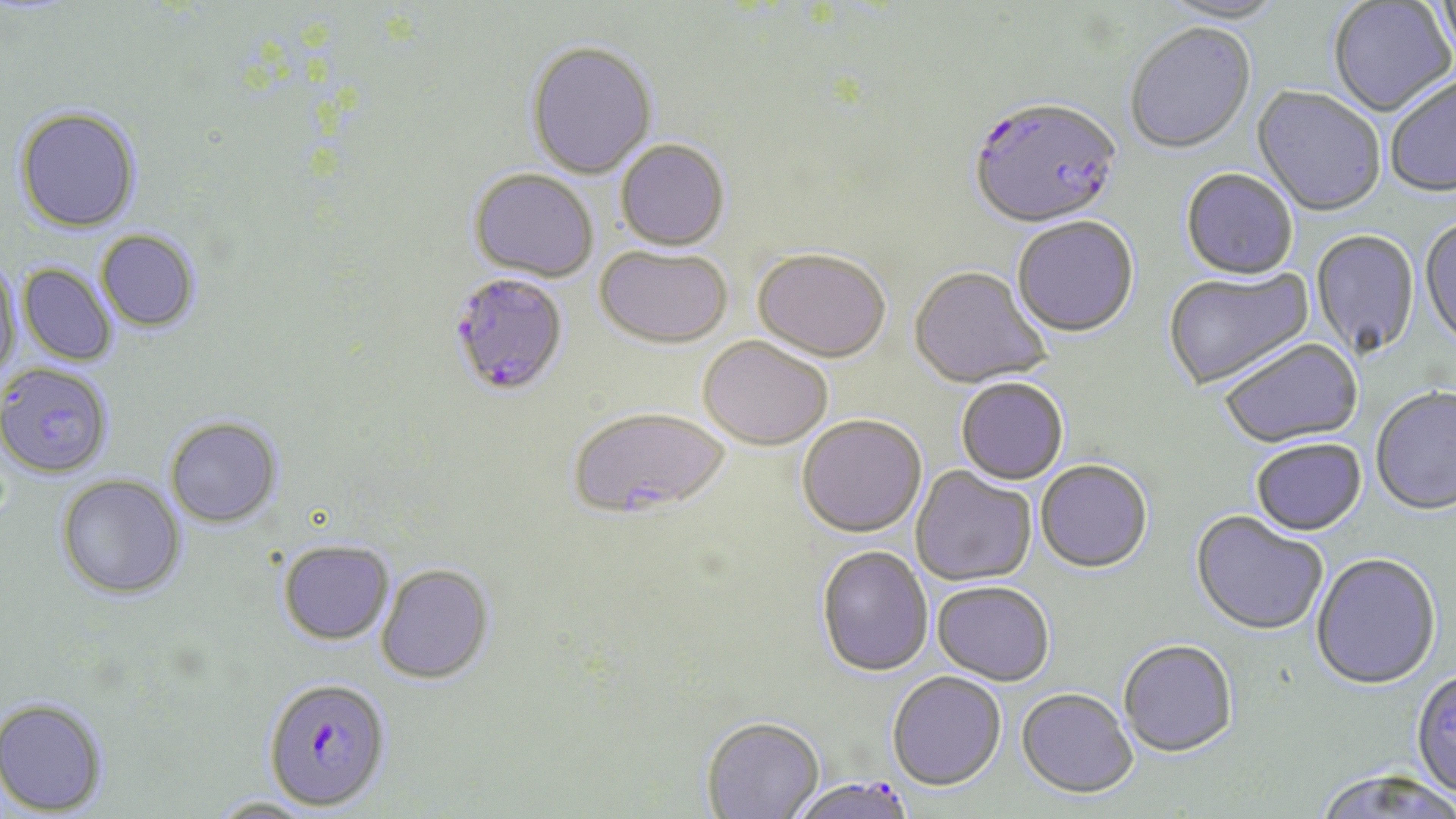
{
  "slide_level_diagnosis": "Plasmodium falciparum",
  "modality": "optical microscopy",
  "stain": "May-Grünwald-Giemsa",
  "field_of_view": "one of a larger specimen",
  "plasmodium_falciparum_infected_red_blood_cell_locations": "approximate bounding boxes as named x1/y1/x2/y2 corners in pixels: (x1=968, y1=99, x2=1122, y2=231), (x1=448, y1=272, x2=570, y2=397), (x1=262, y1=678, x2=392, y2=812), (x1=790, y1=775, x2=921, y2=819)",
  "image_size": "1456×819 pixels",
  "magnification": "1000x",
  "preparation": "thin blood smear",
  "uninfected_red_blood_cell_locations": "approximate bounding boxes as named x1/y1/x2/y2 corners in pixels: (x1=1158, y1=0, x2=1288, y2=26), (x1=1328, y1=1, x2=1455, y2=118), (x1=1432, y1=1, x2=1456, y2=69), (x1=1125, y1=25, x2=1257, y2=156), (x1=525, y1=39, x2=658, y2=179), (x1=1385, y1=76, x2=1456, y2=200), (x1=1251, y1=88, x2=1385, y2=218), (x1=14, y1=105, x2=142, y2=233), (x1=615, y1=139, x2=730, y2=251), (x1=469, y1=168, x2=600, y2=282), (x1=1181, y1=170, x2=1299, y2=282), (x1=1419, y1=217, x2=1456, y2=353), (x1=1012, y1=218, x2=1139, y2=339), (x1=96, y1=229, x2=201, y2=333), (x1=1311, y1=231, x2=1420, y2=360), (x1=595, y1=246, x2=732, y2=349), (x1=752, y1=251, x2=890, y2=364), (x1=0, y1=258, x2=22, y2=379), (x1=17, y1=264, x2=118, y2=366), (x1=908, y1=268, x2=1051, y2=391), (x1=1163, y1=268, x2=1315, y2=392), (x1=697, y1=337, x2=832, y2=452), (x1=1219, y1=339, x2=1363, y2=449), (x1=0, y1=363, x2=114, y2=478), (x1=956, y1=379, x2=1069, y2=486), (x1=1370, y1=388, x2=1456, y2=517), (x1=567, y1=407, x2=730, y2=520), (x1=164, y1=416, x2=283, y2=527), (x1=796, y1=416, x2=927, y2=538), (x1=1251, y1=440, x2=1368, y2=538), (x1=1036, y1=461, x2=1153, y2=575), (x1=910, y1=466, x2=1037, y2=587), (x1=56, y1=474, x2=186, y2=600), (x1=1190, y1=512, x2=1328, y2=637), (x1=277, y1=539, x2=394, y2=645), (x1=816, y1=546, x2=933, y2=678), (x1=1311, y1=555, x2=1442, y2=691), (x1=375, y1=563, x2=494, y2=685), (x1=932, y1=581, x2=1054, y2=687), (x1=1118, y1=641, x2=1237, y2=758), (x1=1410, y1=668, x2=1456, y2=801), (x1=887, y1=672, x2=1007, y2=792), (x1=1016, y1=688, x2=1137, y2=800), (x1=0, y1=697, x2=109, y2=816), (x1=701, y1=716, x2=825, y2=818), (x1=1312, y1=770, x2=1455, y2=819), (x1=208, y1=797, x2=320, y2=818)"
}